Report the malaria status of this cell.
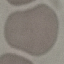

It is uninfected.

Cell patch, automatically extracted from a larger field of view and resized to 64 × 64 pixels. Thin blood smear. Giemsa stain. Acquired by smartphone through the microscope eyepiece.